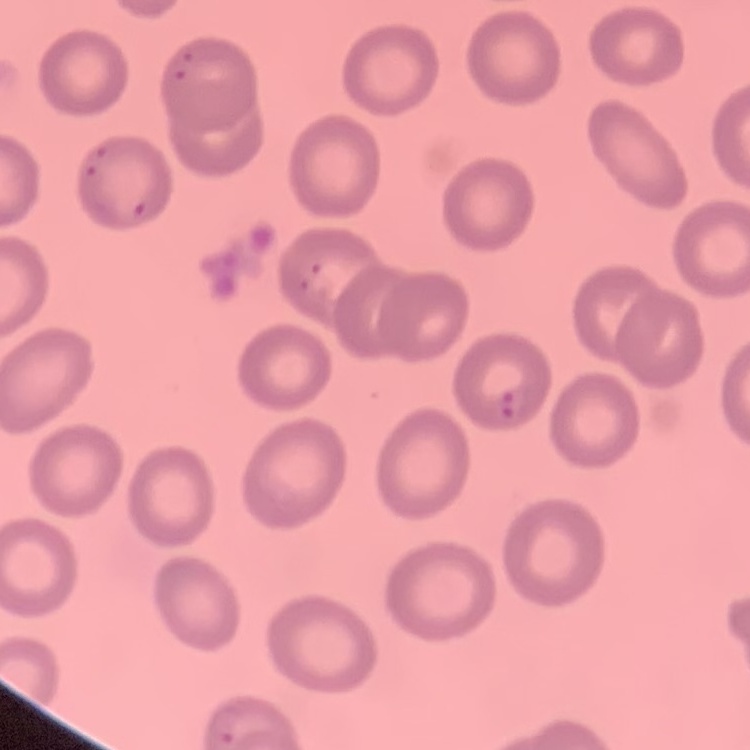 The red blood cells exhibit no rouleaux formation. Square crop of a larger photomicrograph. Stained with either Field's or Giemsa. Thin blood film.